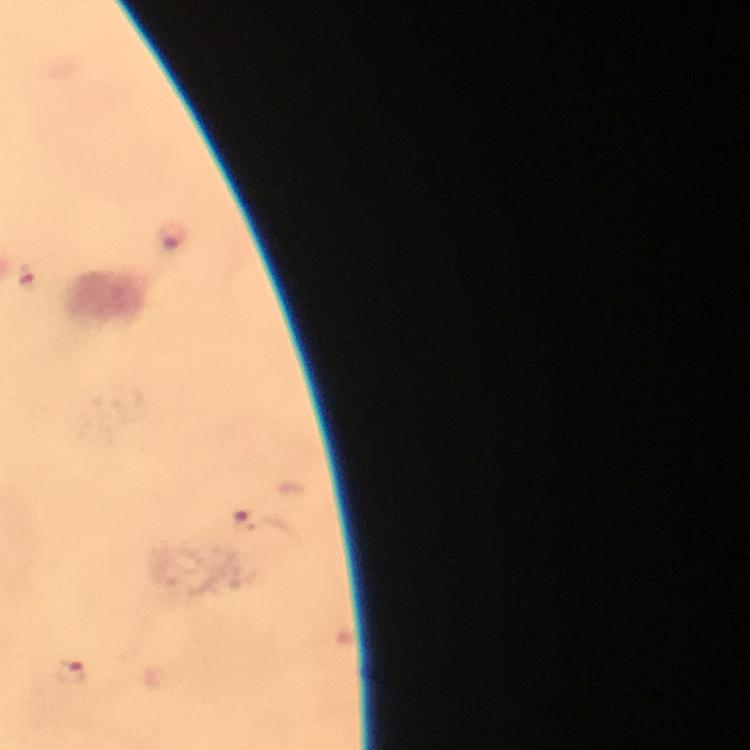
Approximate centers as (x, y) in pixels. Malaria parasite locations: (171, 234), (242, 520), (72, 671). At 100x magnification. Photographed through the microscope with a smartphone camera. A crop from one field of view. Immersion oil was used. Giemsa stain. Thick smear. Image is 750×750 pixels. From a malaria diagnostic workup.